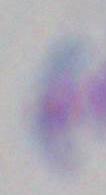

Summary:
  - Modality: micrograph
  - Identification: Toxoplasma gondii
  - Magnification: 1000x